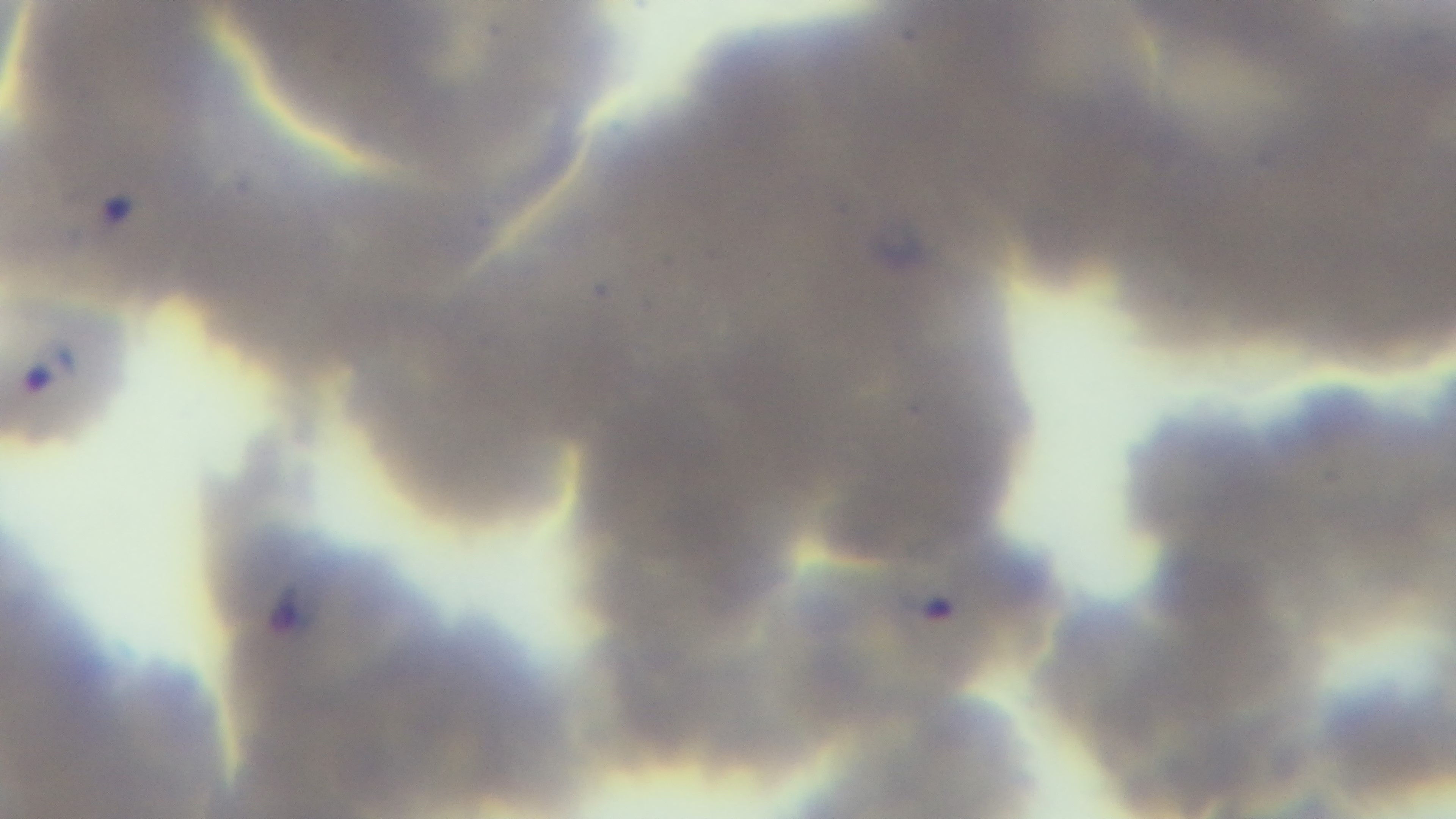
{
  "preparation": "thin blood film",
  "stain": "Giemsa",
  "capture": "mounted 4K digital camera",
  "objective": "100x oil immersion",
  "field_of_view": "one from the slide",
  "malaria_status": "infected",
  "modality": "light microscopy"
}